Point out each malaria parasite.
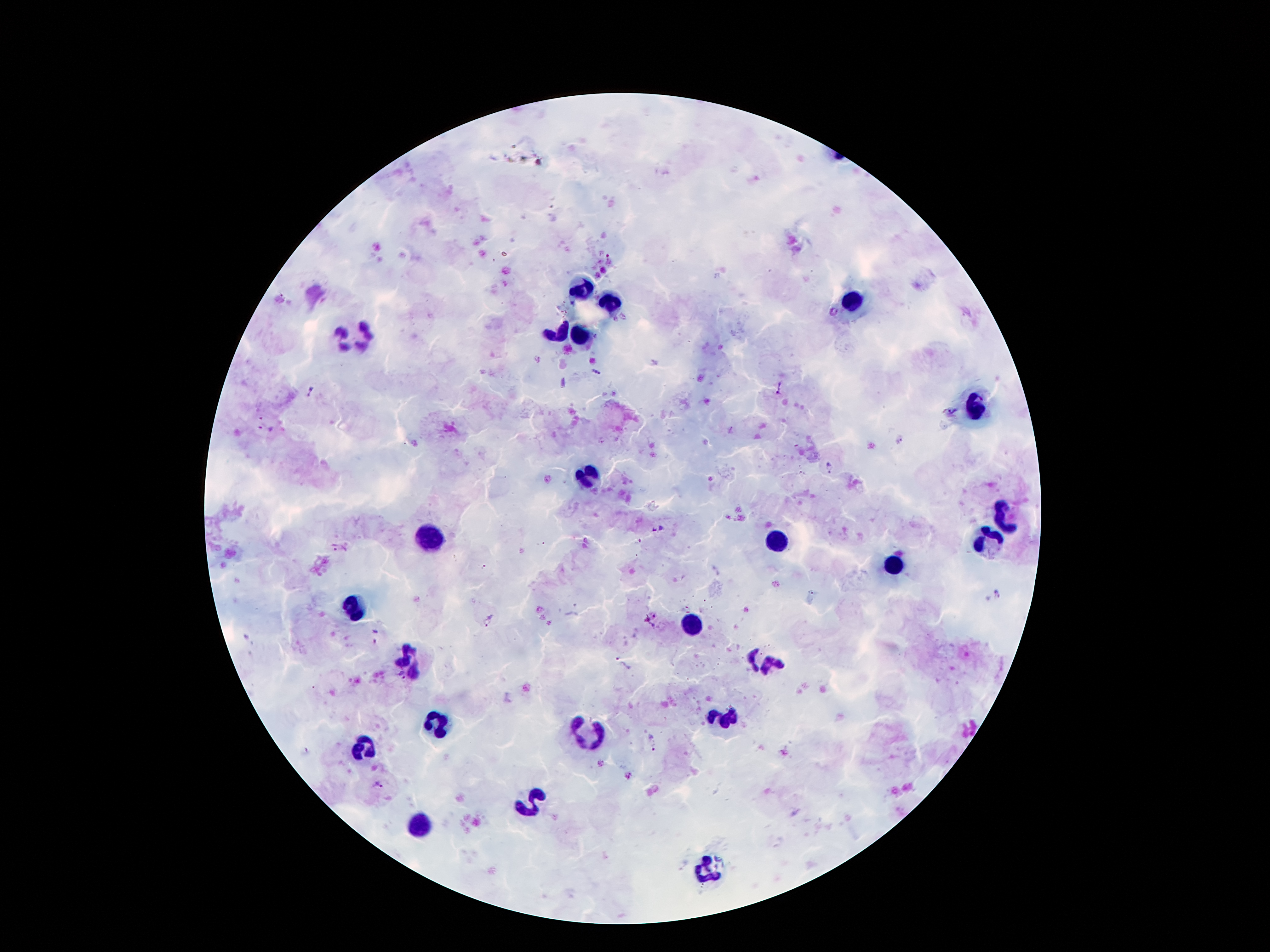
Approximate object centers, in pixels from the top-left corner.
Malaria parasites: (x=834, y=312), (x=594, y=371), (x=779, y=388), (x=311, y=390), (x=952, y=411), (x=831, y=467), (x=658, y=529), (x=334, y=547), (x=1000, y=593), (x=488, y=620), (x=376, y=636), (x=622, y=665), (x=401, y=676), (x=652, y=741), (x=380, y=785).

Leukocyte locations: (x=584, y=287), (x=852, y=301), (x=604, y=302), (x=557, y=334), (x=354, y=337), (x=584, y=337), (x=976, y=411), (x=591, y=473), (x=1006, y=517), (x=431, y=538), (x=992, y=540), (x=779, y=542), (x=892, y=567), (x=356, y=607), (x=692, y=624), (x=409, y=661), (x=764, y=663), (x=725, y=716), (x=440, y=720), (x=586, y=735), (x=366, y=747), (x=530, y=802), (x=419, y=827), (x=707, y=868). Image is 1270×952 pixels. Giemsa-stained preparation. Photographed through the microscope eyepiece with a smartphone camera. 100x magnification. Thick blood film. Single field of view. Patient malaria status: infected with Plasmodium falciparum.